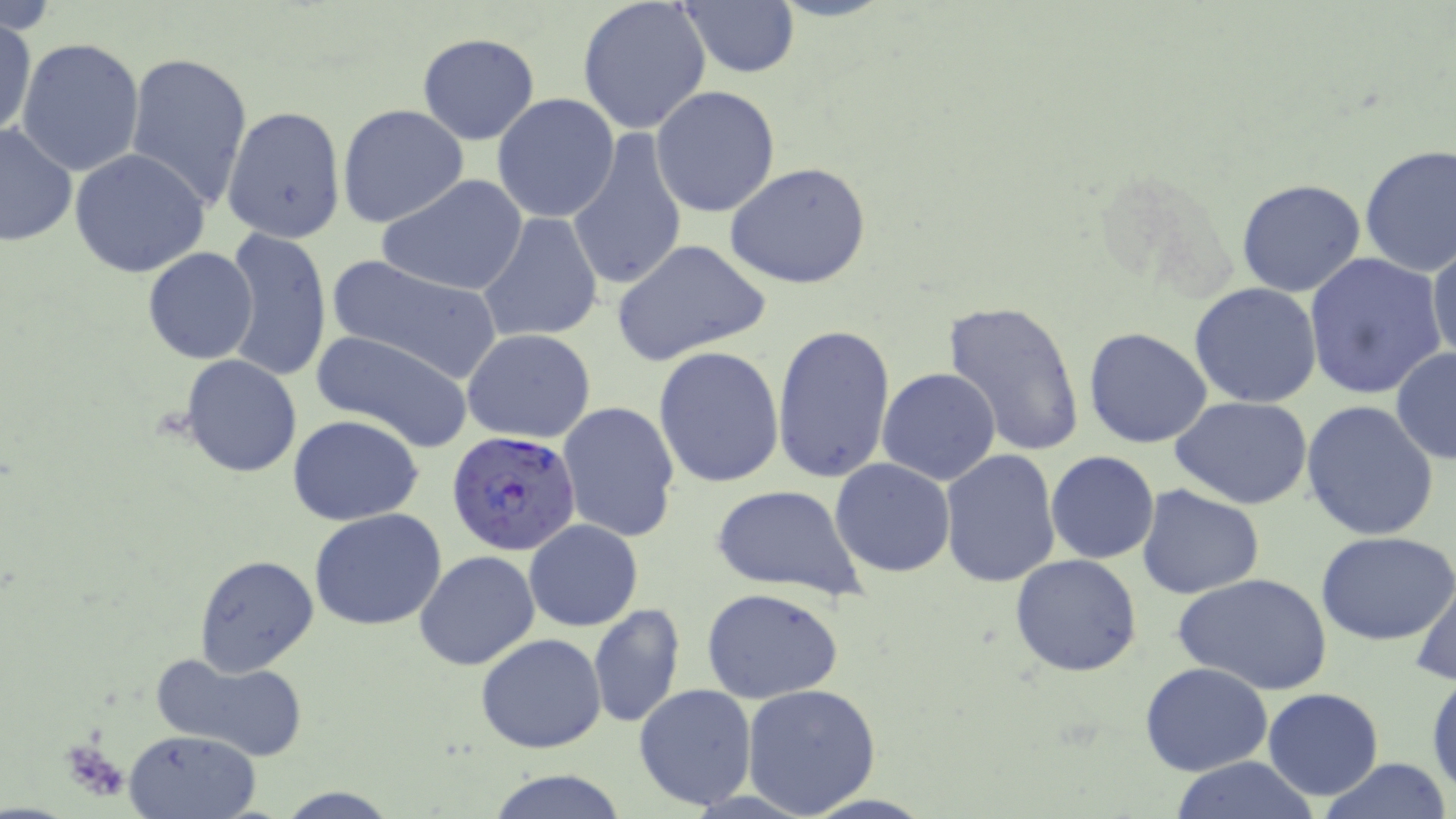 Approximate bounding boxes as [x1, y1, x2, y2] in pixels. Uninfected red blood cell locations: [577, 0, 713, 137], [675, 2, 801, 79], [0, 13, 37, 140], [416, 32, 540, 145], [16, 36, 145, 176], [361, 48, 495, 192], [124, 50, 254, 210], [651, 85, 781, 217], [491, 93, 620, 224], [337, 104, 470, 230], [223, 106, 346, 246], [0, 123, 76, 247], [568, 127, 687, 294], [1358, 145, 1456, 276], [70, 149, 210, 279], [725, 162, 871, 289], [378, 174, 529, 296], [1236, 179, 1368, 298], [476, 213, 606, 345], [223, 228, 332, 380], [611, 240, 772, 365], [1428, 241, 1456, 370], [143, 247, 260, 364], [1302, 252, 1447, 400], [325, 255, 502, 384], [1190, 283, 1323, 407], [942, 300, 1087, 457], [1086, 302, 1320, 429], [771, 323, 894, 486], [1084, 326, 1214, 449], [311, 329, 476, 453], [462, 329, 597, 443], [653, 347, 786, 488], [1390, 347, 1455, 466], [179, 354, 303, 478], [878, 366, 1001, 484], [1172, 396, 1314, 509], [1301, 400, 1441, 541], [556, 401, 681, 544], [287, 414, 424, 526], [939, 450, 1061, 588], [1045, 451, 1160, 564], [830, 457, 955, 578], [711, 485, 865, 602], [1136, 485, 1265, 600], [309, 507, 447, 631], [524, 519, 642, 632], [1317, 530, 1455, 646], [414, 550, 540, 671], [193, 554, 320, 678], [1011, 554, 1143, 676], [1171, 572, 1333, 696], [1410, 575, 1456, 689], [700, 586, 844, 704], [589, 603, 684, 728], [475, 634, 606, 754], [149, 652, 308, 760], [1139, 662, 1272, 776], [1428, 672, 1456, 798], [1136, 676, 1381, 793], [633, 682, 759, 811], [741, 682, 883, 817], [1263, 687, 1383, 800], [122, 729, 261, 818], [1168, 757, 1322, 818], [1318, 758, 1452, 819], [483, 771, 628, 819], [275, 786, 398, 817]. Plasmodium falciparum-infected red blood cell locations: [448, 429, 582, 557]. Slide-level diagnosis: Plasmodium falciparum. Thin blood smear. Captured at 1000x magnification. May-Grünwald-Giemsa-stained preparation. Light microscopy. Single field of view. Image is 1456×819 pixels.